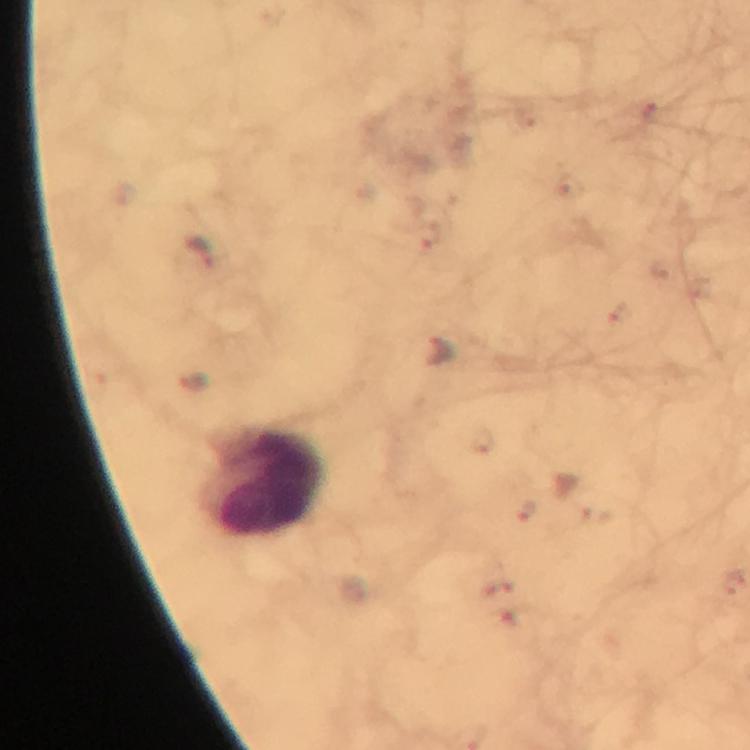

malaria parasite locations = approximate object centers, in pixels from the top-left corner: (x=648, y=112), (x=568, y=186), (x=429, y=235), (x=201, y=252), (x=616, y=312), (x=439, y=352), (x=482, y=440), (x=526, y=510)
capture = smartphone camera through the microscope
cropped from = a single field of view
stain = Giemsa
immersion oil = used
leukocyte locations = approximate object centers, in pixels from the top-left corner: (x=266, y=483)
context = from a diagnostic examination for malaria
image size = 750×750 pixels
magnification = 100x
preparation = thick blood film